Comment on the morphology of the erythrocytes.
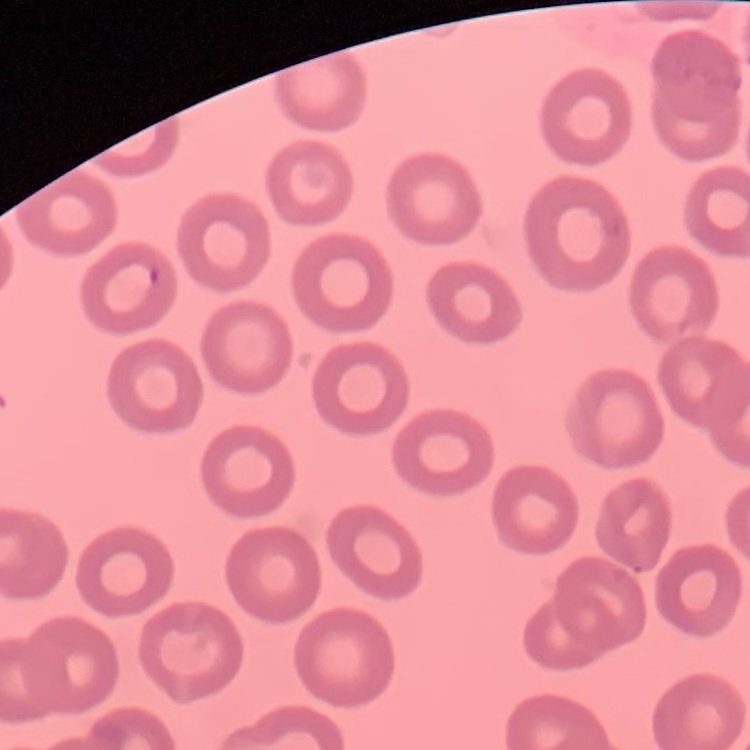
They show no rouleaux formation.

preparation: thin blood smear
stain: Field's or Giemsa
image_type: one tile cut from a larger photomicrograph